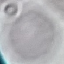

Result: no malaria parasites seen. Cell patch, automatically extracted from a larger field of view and resized to 64 × 64 pixels. Photographed with a smartphone camera at the microscope eyepiece. Thin blood film. Giemsa-stained preparation.